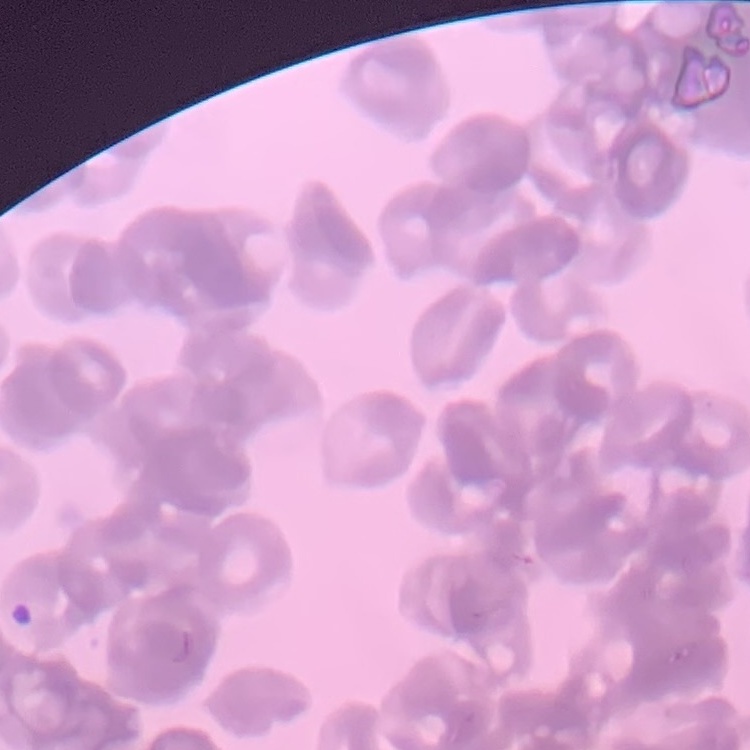
The erythrocytes exhibit rouleaux formation. Square crop of a larger photomicrograph. Stained with either Field's or Giemsa. Thin blood film.